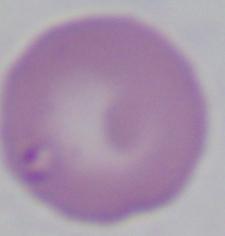
modality: micrograph
magnification: 1000x
identification: Babesia